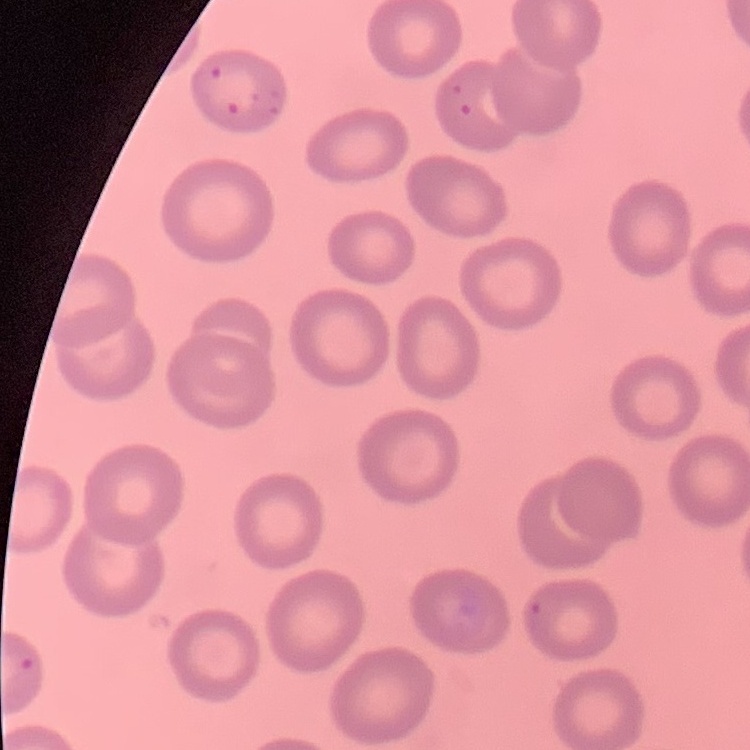

Summary:
  - Red blood cell morphology: no rouleaux formation
  - Image type: one tile cut from a larger photomicrograph
  - Stain: Field's or Giemsa
  - Preparation: thin blood film